Comment on the morphology of the erythrocytes.
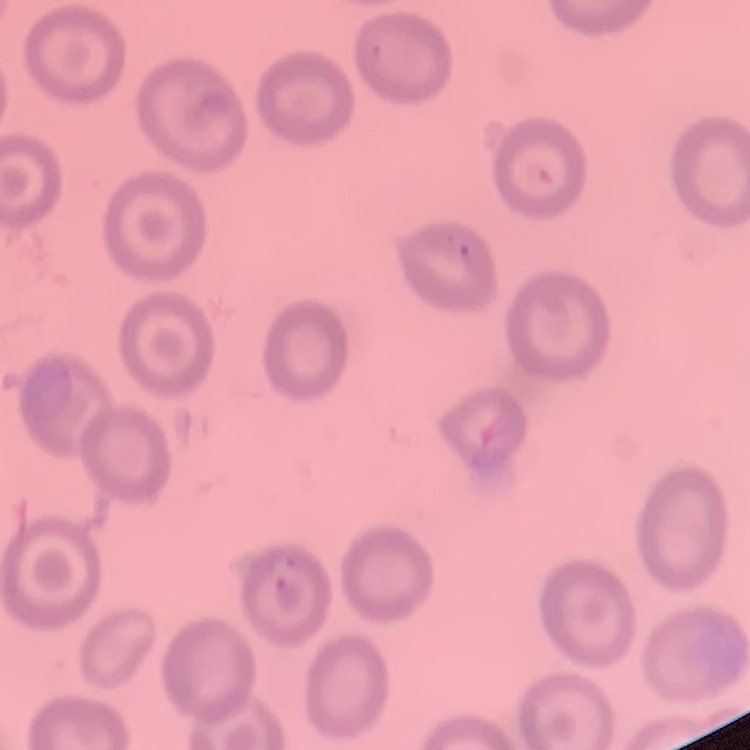

No rouleaux formation.

Field's or Giemsa stain. Thin peripheral smear. Square crop of a larger photomicrograph.